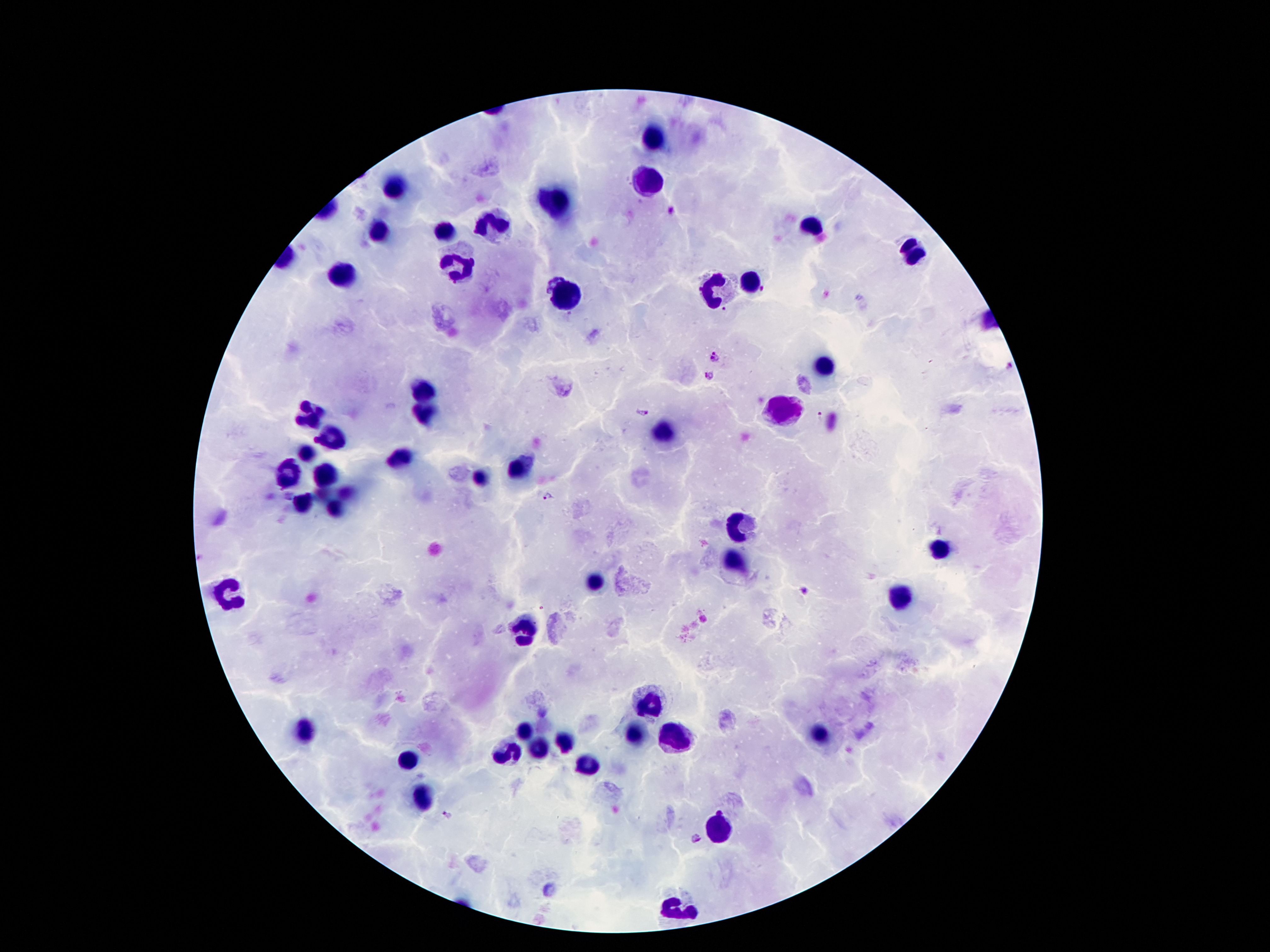
coordinate format = approximate centers as (x, y) in pixels
malaria parasite locations = (671, 214), (715, 358), (708, 376), (642, 411), (819, 415), (547, 495), (802, 590), (448, 815), (695, 836)
leukocyte locations = (653, 133), (644, 181), (395, 187), (559, 202), (499, 219), (811, 226), (448, 231), (377, 234), (914, 255), (457, 267), (343, 273), (751, 282), (716, 292), (566, 295), (823, 366), (424, 390), (782, 409), (425, 411), (311, 418), (665, 432), (332, 438), (305, 453), (398, 460), (518, 469), (289, 471), (326, 478), (480, 479), (301, 505), (734, 525), (938, 550), (737, 562), (595, 577), (227, 594), (899, 598), (521, 631), (649, 706), (304, 732), (521, 733), (674, 735), (635, 736), (820, 736), (565, 742), (535, 751), (506, 754), (406, 763), (586, 766), (422, 796), (718, 832), (679, 910)
magnification = 100x
image size = 1270×952 pixels
preparation = thick peripheral-blood smear
capture = smartphone through the microscope eyepiece
stain = Giemsa
patient malaria status = infected with Plasmodium falciparum
field of view = one from this slide